Assess the morphology of the erythrocytes.
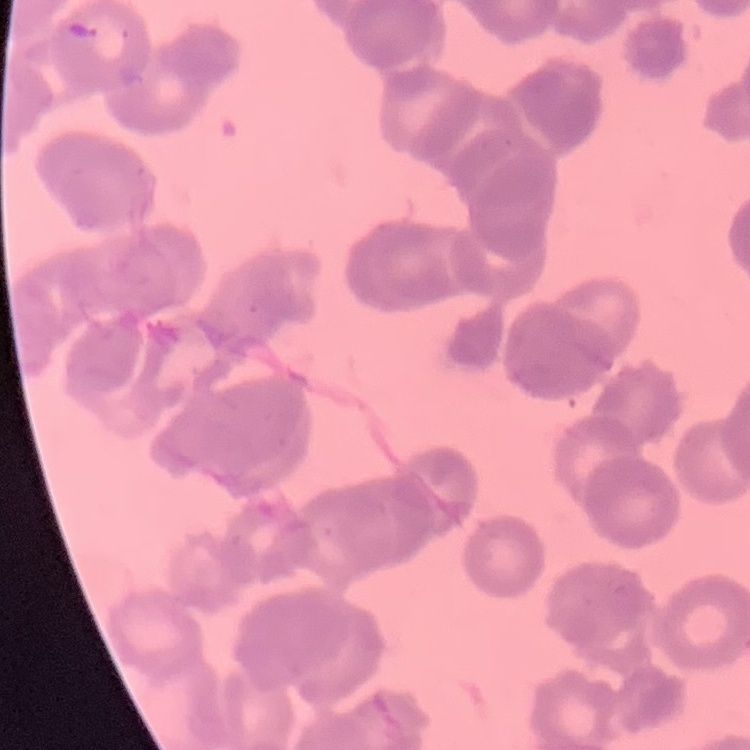

Rouleaux formation.

Summary:
  - Image type: square crop of a larger photomicrograph
  - Preparation: thin blood smear
  - Stain: Field's or Giemsa